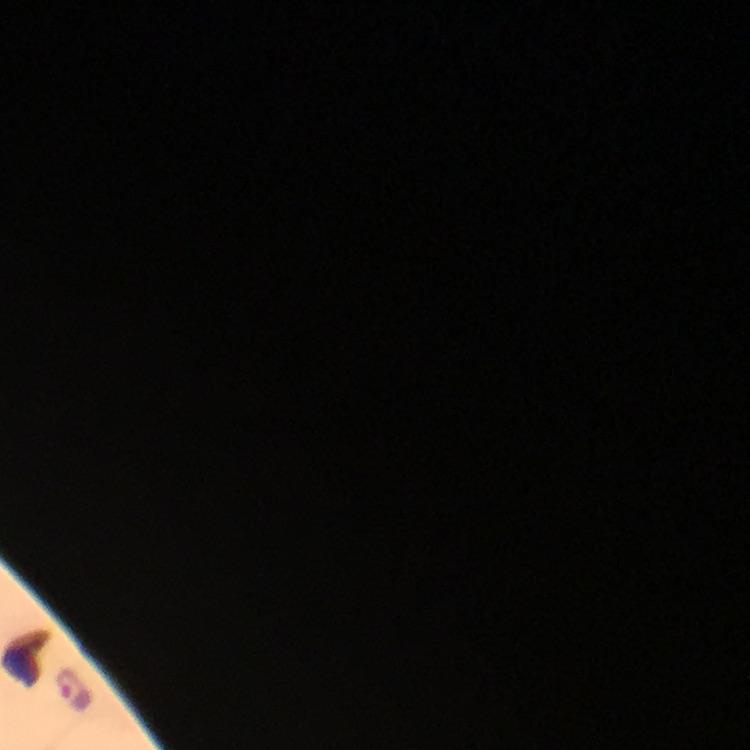

Approximate object centers, in pixels from the top-left corner.
Summary:
  - Plasmodium parasite locations: (x=72, y=690)
  - Capture: smartphone mounted on the microscope
  - Context: from a diagnostic examination for malaria
  - Image size: 750×750 pixels
  - Cropped from: a single field of view
  - Preparation: thick smear
  - Magnification: 100x
  - Stain: Giemsa
  - Immersion oil: used